Name the cell type shown.
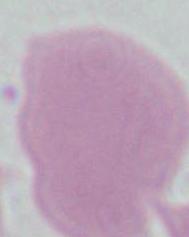

This is an erythrocyte.

Summary:
  - Modality: micrograph
  - Magnification: 1000x